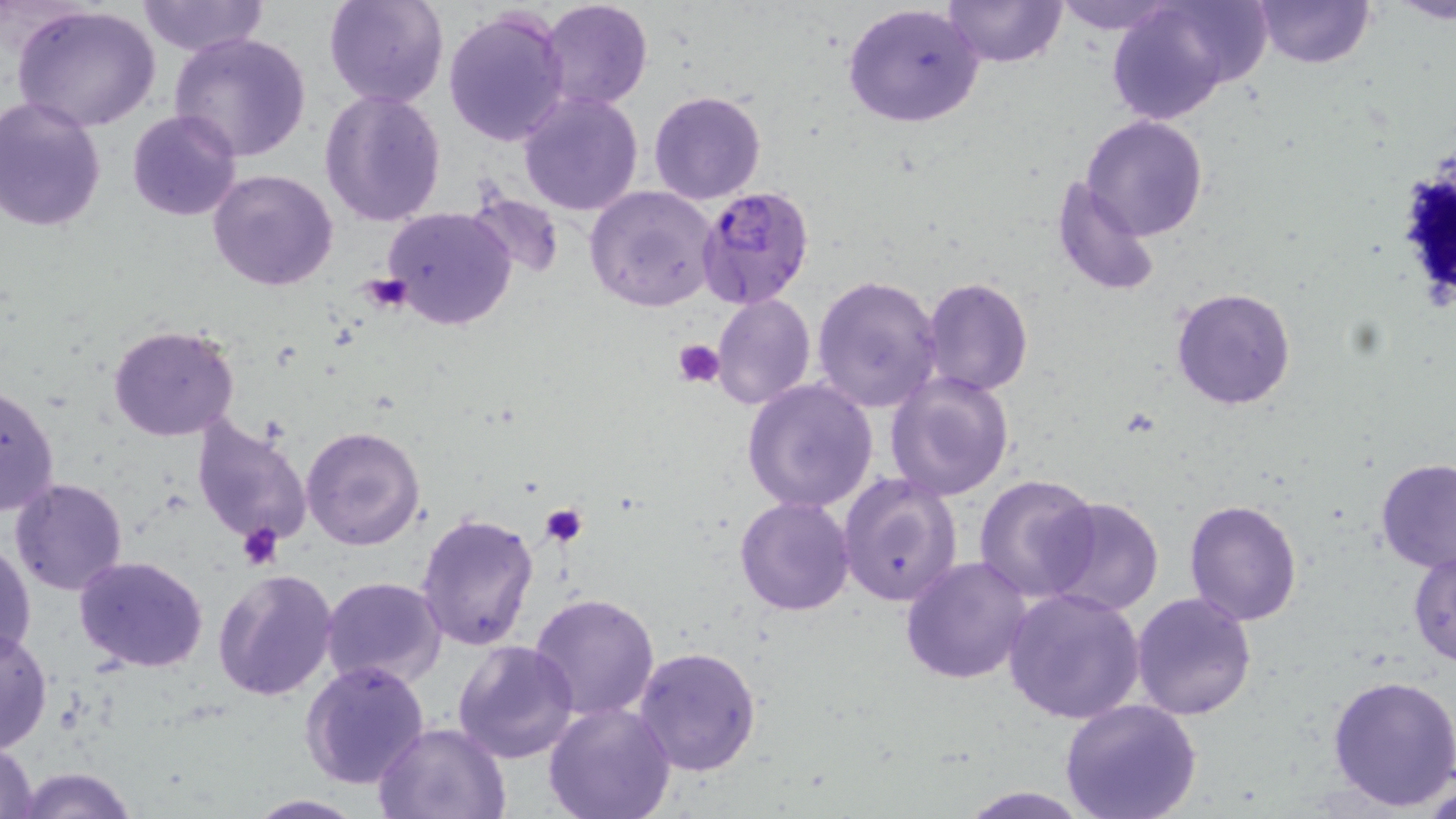

Approximate bounding boxes as (x1,y1)-(x2,y2) corner pairs in pixels. Uninfected red blood cell locations: (324,0)-(450,109), (539,0)-(653,111), (943,0)-(1068,67), (1049,0)-(1184,34), (1254,0)-(1373,68), (1390,0)-(1456,23), (136,1)-(269,56), (1105,1)-(1246,126), (842,3)-(985,128), (14,5)-(160,134), (442,7)-(569,148), (170,31)-(312,161), (319,90)-(446,227), (516,90)-(644,217), (648,91)-(765,204), (0,97)-(108,233), (127,110)-(242,222), (1081,115)-(1207,241), (208,168)-(338,291), (1051,176)-(1163,299), (584,186)-(717,312), (461,187)-(566,280), (381,206)-(517,330), (812,274)-(943,414), (922,277)-(1034,397), (1170,286)-(1296,411), (710,293)-(815,411), (108,323)-(241,443), (885,370)-(1015,502), (740,379)-(880,514), (0,383)-(59,517), (189,410)-(314,551), (301,424)-(426,551), (1376,459)-(1455,571), (974,473)-(1102,603), (839,474)-(963,608), (9,477)-(129,595), (1043,495)-(1163,616), (734,496)-(855,617), (1183,497)-(1303,625), (416,512)-(540,651), (1,542)-(36,661), (1409,545)-(1456,666), (74,555)-(209,673), (900,555)-(1034,684), (213,566)-(339,702), (320,576)-(446,691), (1003,586)-(1147,724), (530,592)-(661,721), (1132,592)-(1257,720), (0,629)-(52,752), (452,639)-(580,764), (633,645)-(763,778), (300,661)-(431,790), (1326,675)-(1456,810), (1059,699)-(1201,819), (542,700)-(676,819), (375,721)-(514,818), (0,739)-(40,819), (12,768)-(141,819), (949,785)-(1099,818), (243,793)-(367,818). Plasmodium falciparum-infected red blood cell locations: (696,186)-(818,311). Platelet locations: (359,274)-(408,313), (673,338)-(725,388), (540,504)-(586,546), (238,523)-(285,570). Slide-level diagnosis: Plasmodium falciparum. Optical microscopy. Single field of view. May-Grünwald-Giemsa-stained preparation. Image is 1456×819 pixels. Thin blood film. Captured at 1000x magnification.